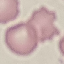
result = no malaria parasites detected
capture = smartphone camera at the microscope eyepiece
preparation = thin smear
stain = Giemsa
image type = cell patch, automatically extracted from a larger field of view and resized to 64 × 64 pixels